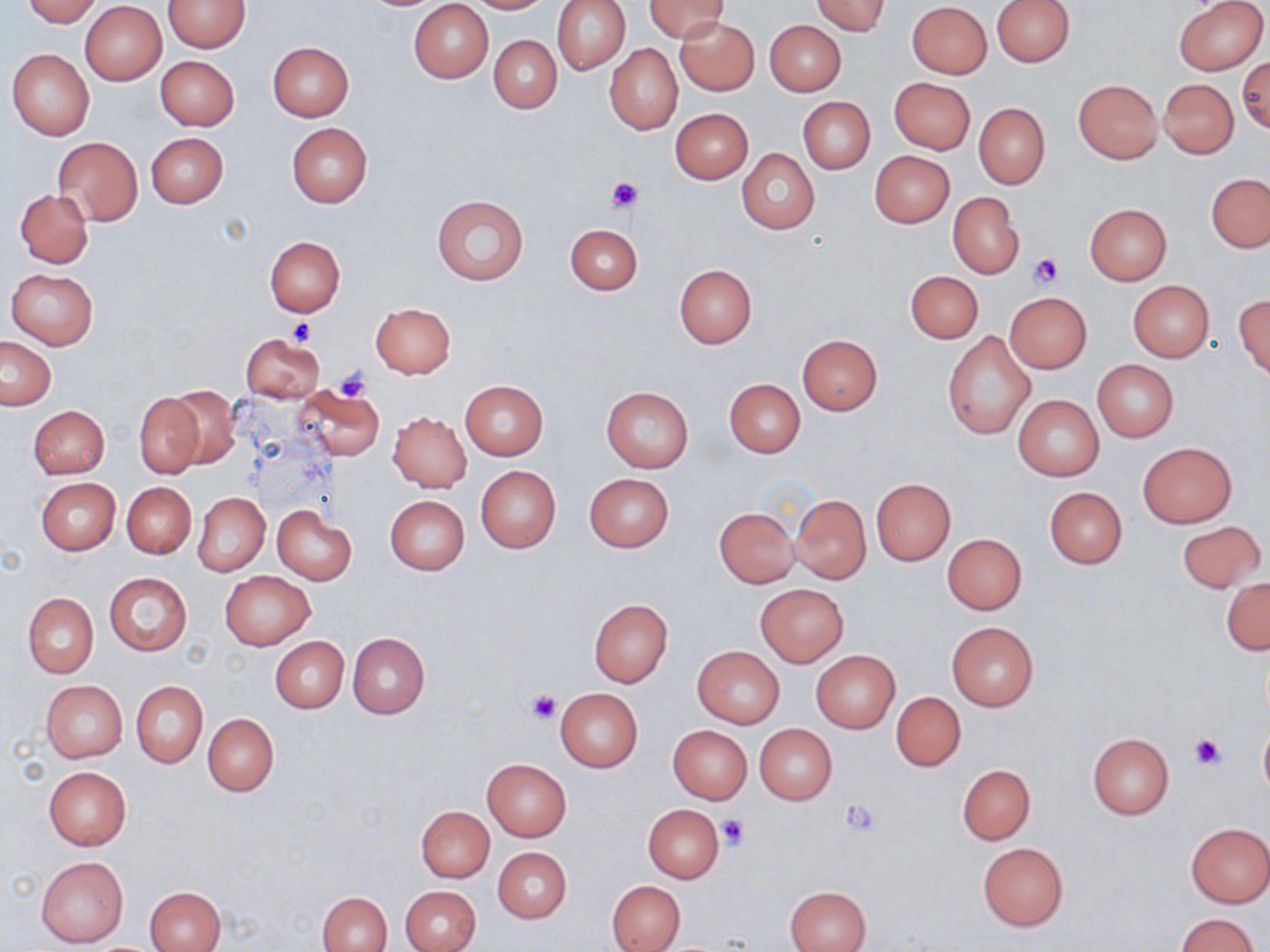
slide-level diagnosis = no evidence of blood parasites
uninfected red blood cell locations = approximate bounding boxes as [x1, y1, x2, y2] in pixels: [24, 0, 100, 26], [465, 0, 555, 13], [552, 0, 631, 75], [645, 0, 730, 42], [811, 0, 891, 36], [991, 0, 1074, 67], [1173, 0, 1268, 75], [163, 1, 250, 53], [408, 1, 493, 82], [80, 2, 167, 85], [906, 2, 993, 80], [676, 17, 760, 95], [765, 20, 846, 95], [488, 34, 562, 113], [267, 42, 354, 122], [605, 44, 682, 135], [7, 49, 95, 140], [155, 56, 239, 130], [1238, 57, 1269, 134], [889, 77, 976, 154], [1072, 79, 1162, 164], [1159, 79, 1239, 158], [797, 96, 875, 174], [974, 103, 1049, 189], [670, 108, 753, 184], [286, 122, 373, 206], [147, 133, 228, 208], [53, 137, 142, 225], [736, 149, 819, 233], [869, 150, 955, 228], [1206, 173, 1270, 252], [14, 189, 93, 267], [948, 193, 1024, 278], [432, 195, 528, 285], [1085, 204, 1172, 285], [565, 222, 642, 295], [264, 236, 345, 317], [674, 264, 757, 348], [7, 269, 97, 349], [906, 271, 983, 343], [1128, 280, 1215, 363], [1004, 293, 1092, 372], [1234, 294, 1270, 379], [369, 303, 457, 378], [942, 331, 1035, 440], [242, 334, 325, 402], [796, 335, 882, 416], [1, 336, 56, 409], [1092, 359, 1177, 442], [724, 378, 805, 457], [460, 380, 549, 459], [295, 385, 383, 461], [166, 386, 241, 469], [601, 386, 694, 472], [134, 393, 204, 478], [1013, 395, 1103, 481], [28, 405, 109, 478], [388, 412, 472, 491], [1138, 441, 1236, 528], [475, 466, 561, 551], [584, 473, 674, 551], [35, 477, 121, 554], [871, 479, 955, 565], [122, 482, 195, 558], [1044, 487, 1126, 569], [193, 493, 269, 576], [384, 495, 470, 575], [790, 495, 870, 583], [272, 506, 356, 584], [715, 507, 801, 587], [1178, 519, 1266, 593], [942, 533, 1026, 615], [220, 570, 315, 651], [104, 572, 192, 656], [1222, 577, 1269, 655], [756, 584, 848, 666], [22, 593, 98, 678], [589, 599, 673, 687], [947, 622, 1038, 710], [347, 632, 430, 718], [271, 636, 349, 713], [692, 646, 785, 728], [811, 650, 901, 733], [40, 680, 126, 763], [131, 681, 207, 767], [555, 687, 643, 773], [891, 691, 965, 771], [203, 713, 280, 797], [1259, 721, 1270, 800], [754, 724, 837, 805], [668, 725, 752, 803], [1088, 733, 1174, 819], [482, 758, 571, 840], [957, 763, 1035, 844], [44, 767, 132, 850], [643, 805, 723, 883], [417, 806, 494, 883], [1185, 822, 1269, 907], [978, 843, 1068, 930], [493, 847, 572, 923], [37, 857, 128, 947], [608, 881, 684, 952], [400, 885, 481, 952], [146, 887, 227, 952], [786, 887, 870, 951], [318, 891, 392, 952], [1177, 913, 1259, 952]
magnification = 1000x
stain = May-Grünwald-Giemsa
preparation = thin blood smear
modality = light microscopy
field of view = single
image size = 1270×952 pixels
platelet locations = approximate bounding boxes as [x1, y1, x2, y2] in pixels: [605, 175, 642, 215], [1027, 254, 1063, 289], [287, 317, 314, 345], [333, 367, 373, 401], [526, 691, 560, 725], [1190, 734, 1225, 772], [840, 800, 881, 836], [716, 815, 750, 850]